Assess this cell for malaria.
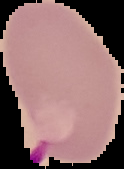
Parasitized.

Summary:
  - Preparation: thin blood smear
  - Image type: segmented cell region on a black background
  - Image size: 124×169 pixels